Give a bounding box for every malaria parasite.
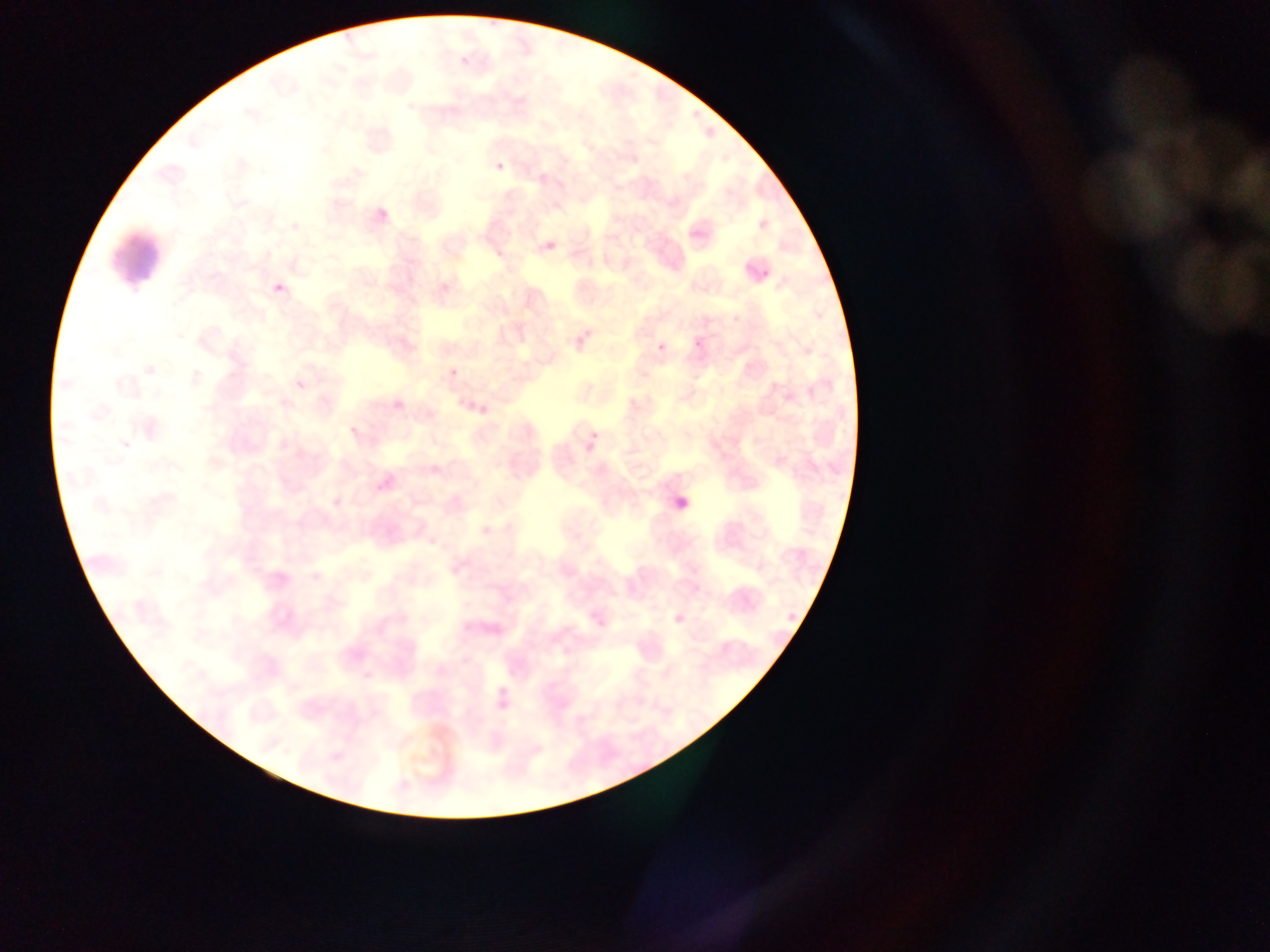
Approximate bounding boxes as {left, top, right, bottom} in pixels.
Malaria parasites: {495, 162, 504, 171}, {379, 209, 387, 219}, {543, 238, 553, 250}, {755, 264, 776, 277}, {274, 273, 297, 290}, {442, 282, 452, 292}, {566, 324, 592, 350}, {653, 336, 673, 355}, {694, 338, 703, 347}, {449, 368, 458, 378}, {478, 405, 490, 420}, {350, 426, 359, 436}, {590, 431, 599, 439}, {670, 599, 696, 629}, {592, 606, 618, 633}.

field of view = single
capture = mobile-phone photograph through a microscope
image size = 1270×952 pixels
preparation = thin blood film
country = Ghana